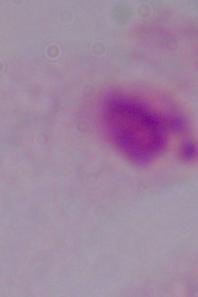
Micrograph. A trichomonad is seen. 1000x magnification.